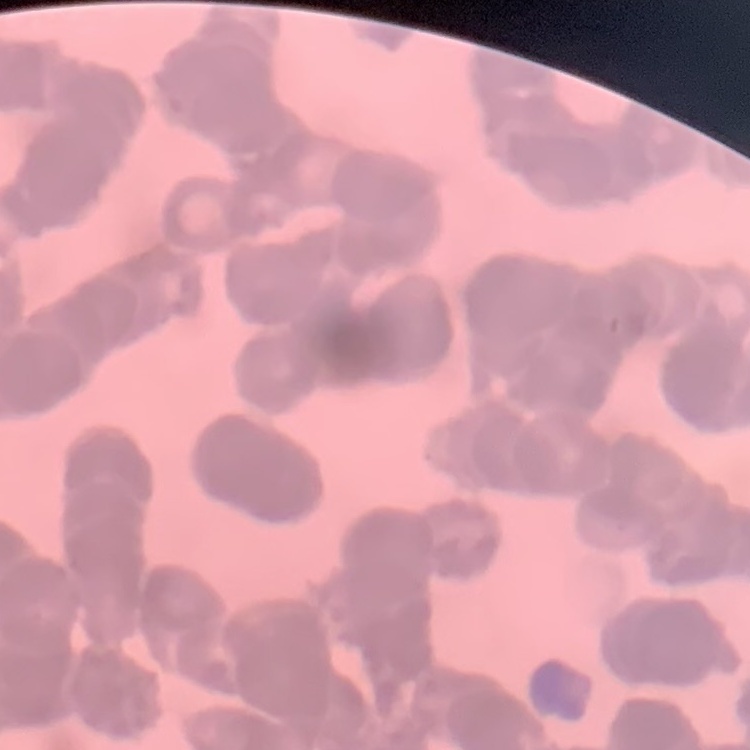 The erythrocytes show rouleaux formation. Thin blood smear. One tile cut from a larger photomicrograph. Stained with either Field's or Giemsa.